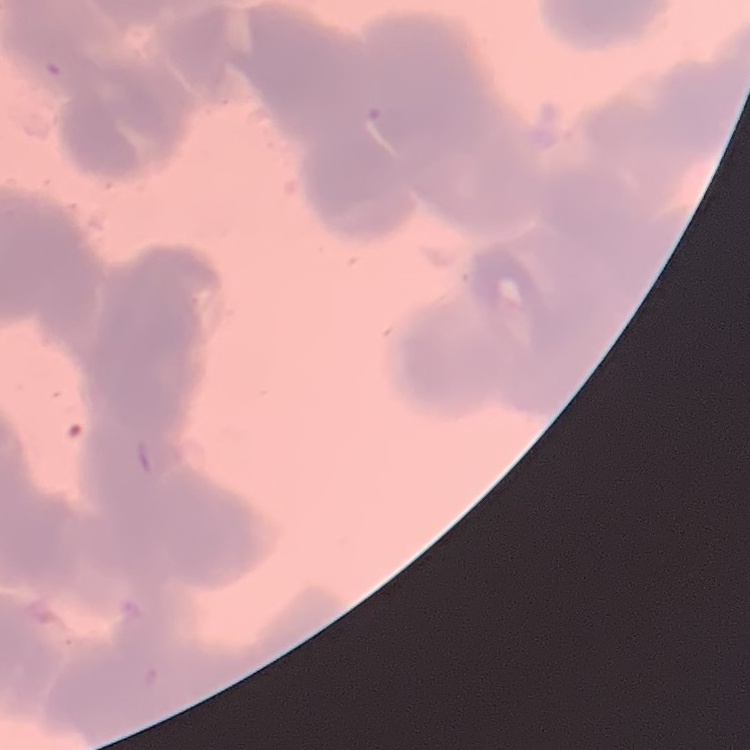 The red blood cells exhibit rouleaux formation. Thin peripheral smear. Stained with either Field's or Giemsa. One tile cut from a larger photomicrograph.